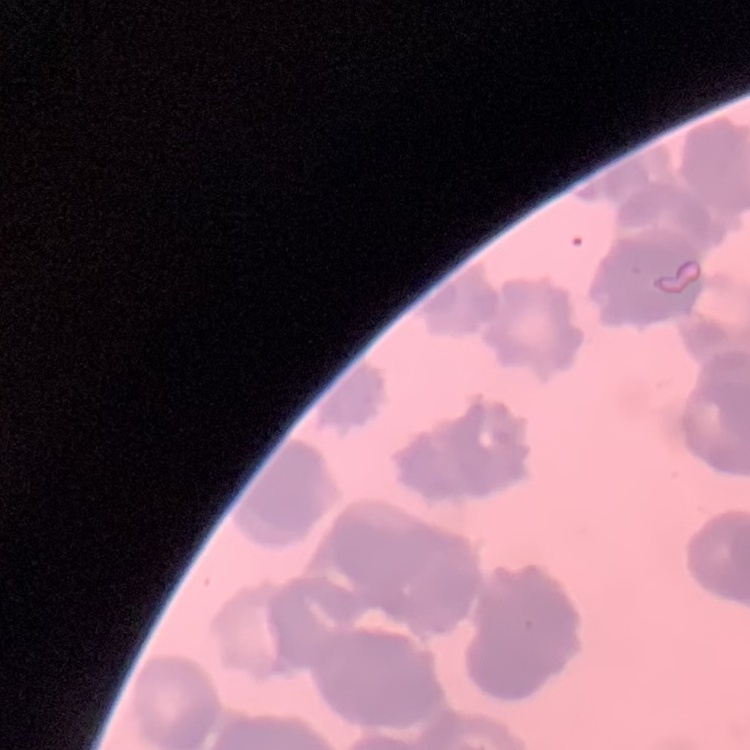 The erythrocytes show rouleaux formation. Stained with either Field's or Giemsa. One tile cut from a larger photomicrograph. Thin blood film.